Report the malaria status of this cell.
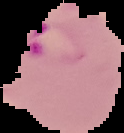

Parasitized.

Summary:
  - Image type: segmented cell region with the area outside set to black
  - Preparation: thin blood smear
  - Image size: 124×133 pixels